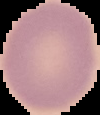

Summary:
  - Image type: segmented cell region on a black background
  - Image size: 100×115 pixels
  - Malaria status: uninfected
  - Preparation: thin blood smear